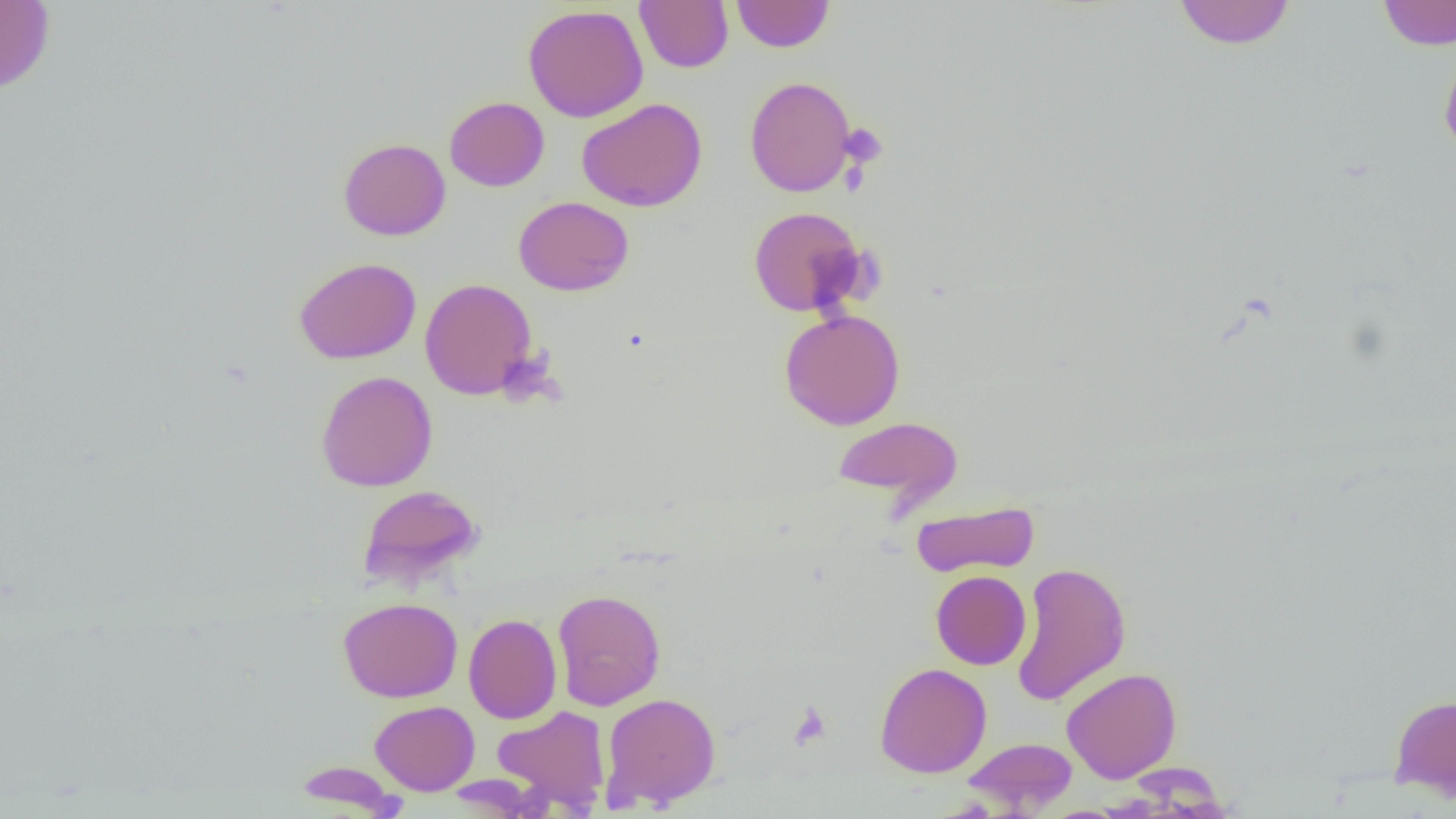

Approximate bounding boxes as named x1/y1/x2/y2 corners in pixels. Platelet locations: (x1=839, y1=122, x2=888, y2=169), (x1=787, y1=701, x2=833, y2=750). Uninfected red blood cell locations: (x1=634, y1=0, x2=733, y2=73), (x1=0, y1=1, x2=54, y2=95), (x1=731, y1=1, x2=835, y2=52), (x1=1173, y1=1, x2=1296, y2=49), (x1=1376, y1=1, x2=1456, y2=50), (x1=522, y1=4, x2=648, y2=122), (x1=1439, y1=44, x2=1456, y2=161), (x1=745, y1=76, x2=856, y2=196), (x1=445, y1=96, x2=549, y2=191), (x1=577, y1=98, x2=707, y2=212), (x1=339, y1=138, x2=451, y2=240), (x1=514, y1=196, x2=634, y2=296), (x1=747, y1=206, x2=867, y2=317), (x1=295, y1=257, x2=421, y2=364), (x1=420, y1=277, x2=537, y2=400), (x1=779, y1=309, x2=905, y2=430), (x1=315, y1=371, x2=438, y2=492), (x1=832, y1=416, x2=963, y2=508), (x1=357, y1=484, x2=484, y2=589), (x1=911, y1=501, x2=1040, y2=578), (x1=1011, y1=560, x2=1131, y2=706), (x1=931, y1=570, x2=1031, y2=670), (x1=552, y1=588, x2=666, y2=710), (x1=338, y1=597, x2=462, y2=702), (x1=463, y1=613, x2=562, y2=724), (x1=874, y1=662, x2=992, y2=778), (x1=1061, y1=667, x2=1182, y2=783), (x1=600, y1=692, x2=722, y2=810), (x1=1390, y1=693, x2=1456, y2=800), (x1=370, y1=700, x2=480, y2=795), (x1=493, y1=705, x2=611, y2=811), (x1=962, y1=737, x2=1078, y2=813), (x1=293, y1=761, x2=403, y2=815). Slide-level diagnosis: no evidence of blood parasites. Light microscopy. Captured at 1000x magnification. One field of a larger specimen. Thin blood smear. Image is 1456×819 pixels.